Assess the morphology of the red blood cells.
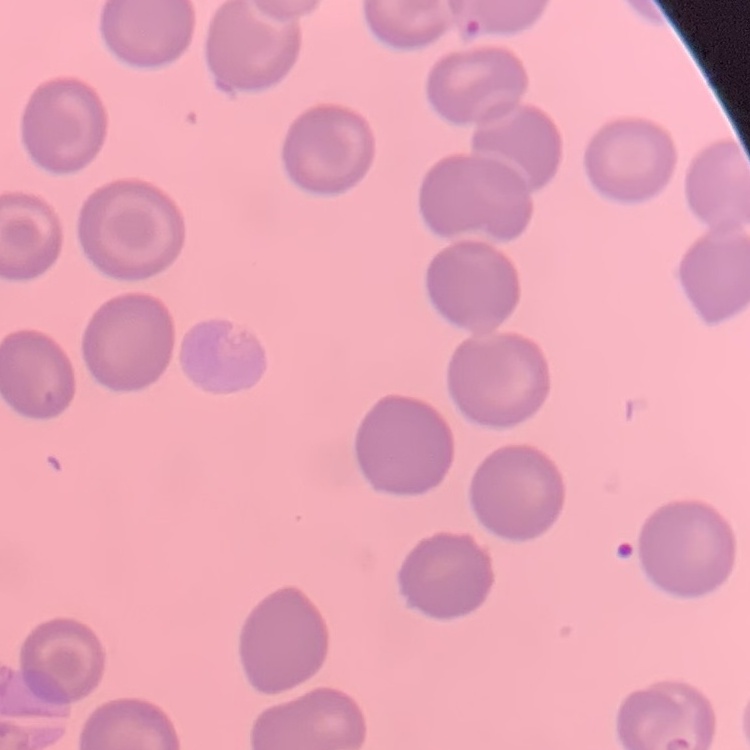
They show no rouleaux formation.

Summary:
  - Image type: square crop of a larger photomicrograph
  - Stain: Field's or Giemsa
  - Preparation: thin peripheral smear